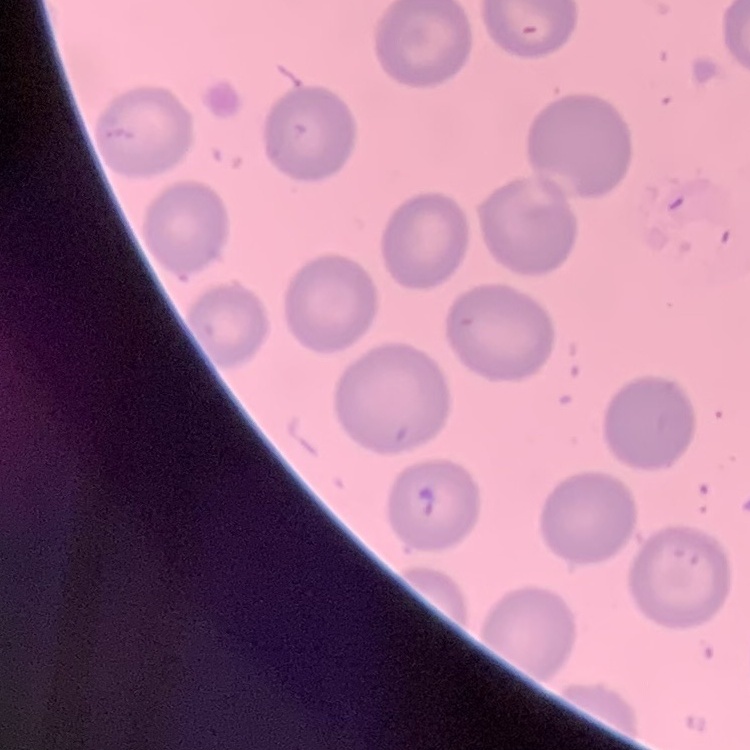
Summary:
  - Erythrocyte morphology: no rouleaux formation
  - Stain: Field's or Giemsa
  - Preparation: thin blood smear
  - Image type: one tile cut from a larger photomicrograph